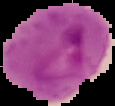

Summary:
  - Image size: 115×106 pixels
  - Image type: segmented cell region with the area outside set to black
  - Preparation: thin blood smear
  - Result: malaria parasites identified